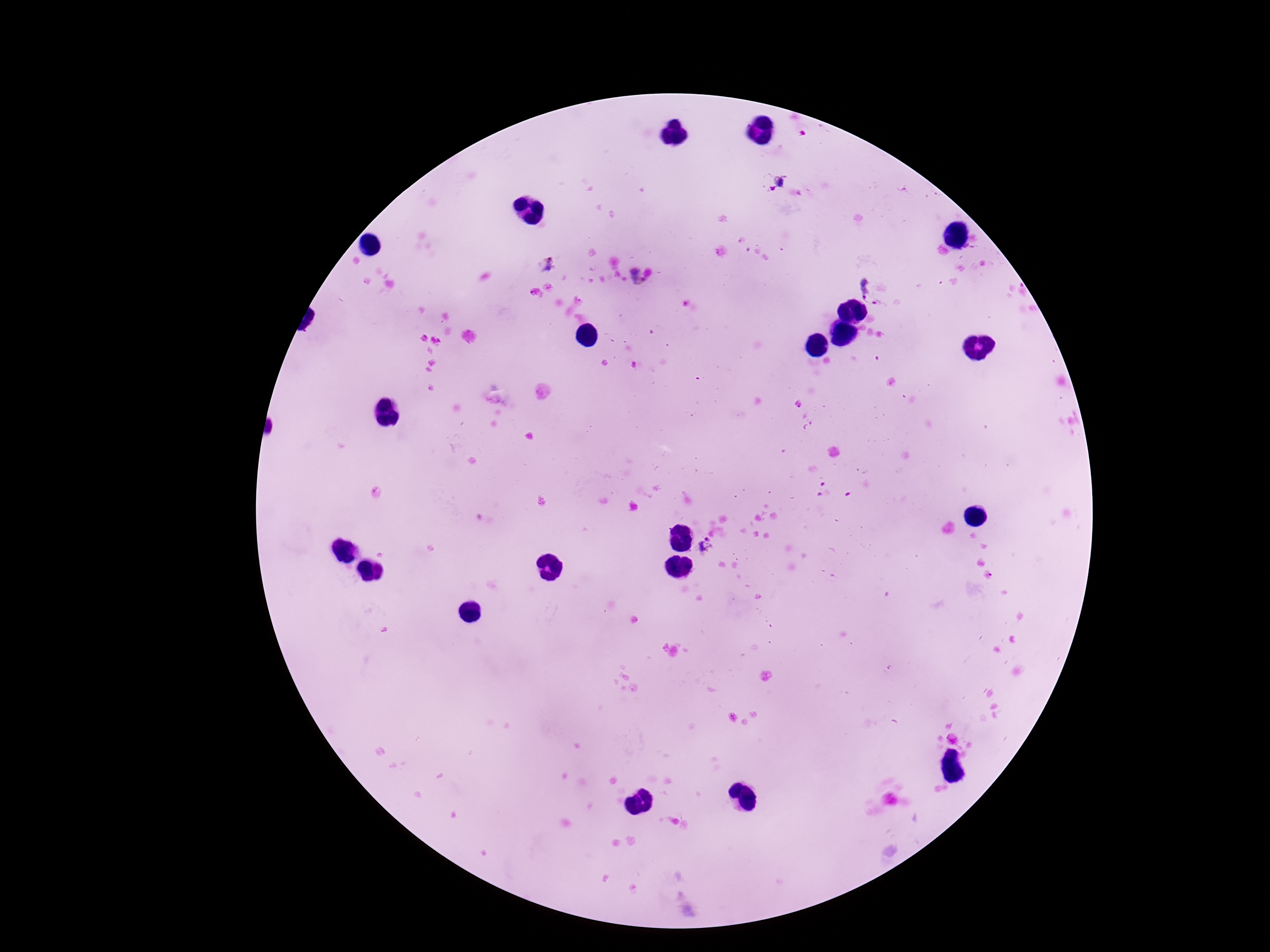
Approximate object centers, in pixels from the top-left corner. Plasmodium parasite locations: (x=779, y=182), (x=548, y=265), (x=637, y=277), (x=874, y=285), (x=707, y=547). Photographed through the microscope eyepiece with a smartphone camera. Single field of view. Image is 1270×952 pixels. Thick blood smear. Patient malaria status: positive. Giemsa-stained preparation. 100x magnification.